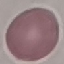 Result: negative for malaria parasites. Acquired by smartphone through the microscope eyepiece. Cell patch, automatically extracted from a larger field of view and resized to 64 × 64 pixels. Thin blood smear. Giemsa stain.